Classify this cell by malaria status.
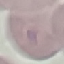
Uninfected.

preparation: thin smear
capture: smartphone through the microscope eyepiece
stain: Giemsa
image_type: cell patch, automatically extracted from a larger field of view and resized to 64 × 64 pixels